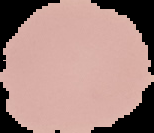 Segmented cell region on a black background. Image is 154×133 pixels. Result: no malaria parasites detected. From a thin blood film.